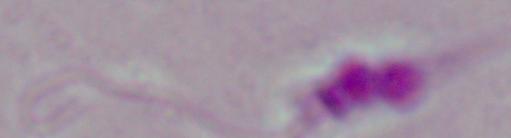
Summary:
  - Magnification: 1000x
  - Identification: Leishmania
  - Modality: photomicrograph